Classify this cell by malaria status.
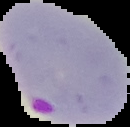

Parasitized.

Summary:
  - Image size: 130×127 pixels
  - Image type: segmented cell region on a black background
  - Preparation: thin blood smear